Describe the morphology of the erythrocytes.
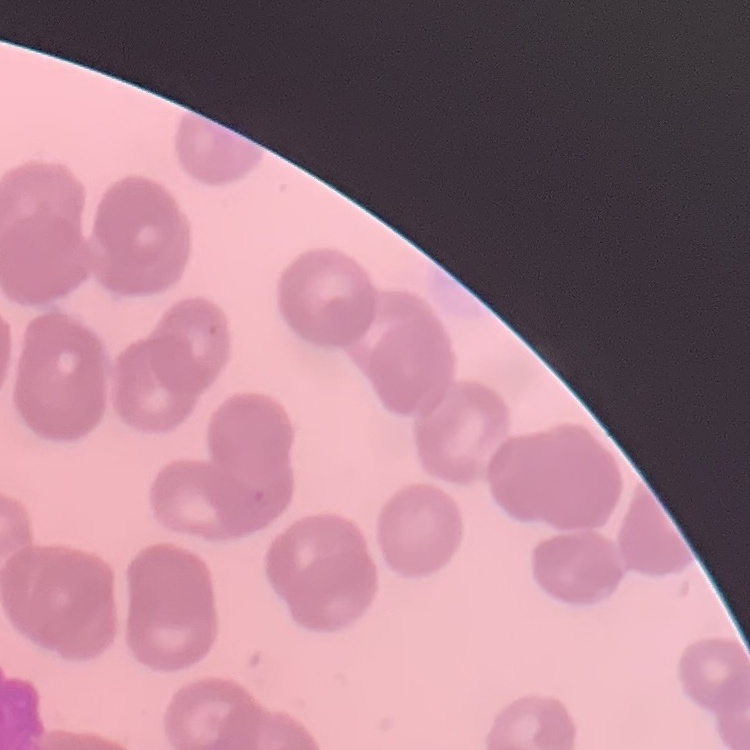
Rouleaux formation.

Field's or Giemsa stain. One tile cut from a larger photomicrograph. Thin blood film.